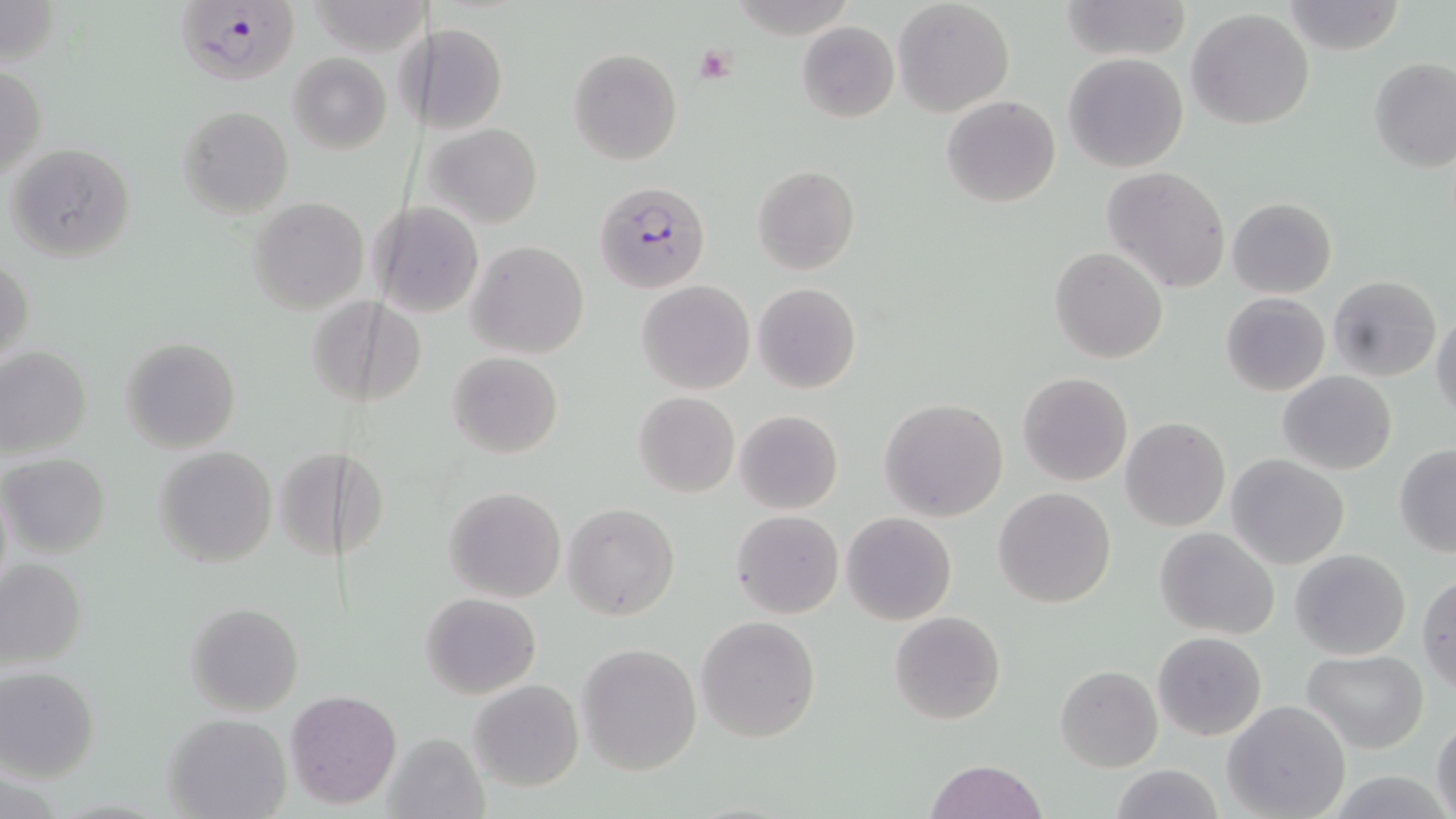 Approximate bounding boxes as named x1/y1/x2/y2 corners in pixels. Uninfected red blood cell locations: (x1=0, y1=0, x2=64, y2=68), (x1=893, y1=0, x2=1015, y2=116), (x1=1058, y1=0, x2=1191, y2=62), (x1=1281, y1=1, x2=1405, y2=54), (x1=1186, y1=8, x2=1316, y2=130), (x1=797, y1=20, x2=899, y2=123), (x1=394, y1=21, x2=427, y2=130), (x1=425, y1=23, x2=508, y2=134), (x1=568, y1=46, x2=683, y2=165), (x1=286, y1=53, x2=393, y2=154), (x1=1062, y1=53, x2=1189, y2=172), (x1=1367, y1=58, x2=1455, y2=172), (x1=1, y1=64, x2=45, y2=180), (x1=941, y1=95, x2=1060, y2=208), (x1=177, y1=104, x2=295, y2=219), (x1=423, y1=121, x2=546, y2=227), (x1=6, y1=142, x2=136, y2=262), (x1=752, y1=164, x2=860, y2=275), (x1=1103, y1=165, x2=1232, y2=293), (x1=248, y1=197, x2=369, y2=315), (x1=1227, y1=198, x2=1337, y2=297), (x1=370, y1=202, x2=485, y2=317), (x1=467, y1=241, x2=589, y2=358), (x1=1050, y1=246, x2=1167, y2=364), (x1=0, y1=256, x2=34, y2=368), (x1=1327, y1=275, x2=1441, y2=383), (x1=638, y1=281, x2=755, y2=395), (x1=753, y1=283, x2=861, y2=395), (x1=1221, y1=291, x2=1330, y2=397), (x1=309, y1=295, x2=425, y2=409), (x1=1431, y1=310, x2=1456, y2=421), (x1=119, y1=337, x2=242, y2=453), (x1=0, y1=346, x2=92, y2=460), (x1=447, y1=352, x2=563, y2=458), (x1=1277, y1=369, x2=1397, y2=475), (x1=1017, y1=372, x2=1133, y2=486), (x1=633, y1=391, x2=740, y2=498), (x1=879, y1=398, x2=1007, y2=522), (x1=734, y1=409, x2=842, y2=514), (x1=1121, y1=417, x2=1230, y2=531), (x1=1394, y1=444, x2=1456, y2=558), (x1=153, y1=446, x2=278, y2=569), (x1=277, y1=447, x2=341, y2=564), (x1=339, y1=448, x2=387, y2=564), (x1=1, y1=453, x2=110, y2=558), (x1=1227, y1=455, x2=1349, y2=569), (x1=442, y1=486, x2=566, y2=603), (x1=994, y1=487, x2=1115, y2=609), (x1=564, y1=502, x2=680, y2=621), (x1=732, y1=510, x2=844, y2=618), (x1=841, y1=512, x2=957, y2=625), (x1=1155, y1=527, x2=1278, y2=640), (x1=1290, y1=549, x2=1411, y2=661), (x1=0, y1=557, x2=87, y2=669), (x1=1418, y1=574, x2=1456, y2=692), (x1=421, y1=592, x2=541, y2=699), (x1=185, y1=601, x2=304, y2=715), (x1=888, y1=611, x2=1006, y2=725), (x1=696, y1=615, x2=821, y2=742), (x1=1153, y1=632, x2=1267, y2=741), (x1=577, y1=642, x2=703, y2=775), (x1=1301, y1=650, x2=1429, y2=754), (x1=1056, y1=665, x2=1162, y2=771), (x1=0, y1=667, x2=101, y2=781), (x1=467, y1=679, x2=585, y2=791), (x1=285, y1=689, x2=401, y2=809), (x1=1223, y1=700, x2=1353, y2=819), (x1=163, y1=711, x2=291, y2=818), (x1=1432, y1=717, x2=1456, y2=819), (x1=380, y1=731, x2=488, y2=819), (x1=924, y1=759, x2=1049, y2=818), (x1=1110, y1=765, x2=1223, y2=819), (x1=1323, y1=771, x2=1455, y2=819). Plasmodium falciparum-infected red blood cell locations: (x1=173, y1=1, x2=298, y2=89), (x1=596, y1=181, x2=710, y2=293). Platelet locations: (x1=692, y1=44, x2=739, y2=85). Slide-level diagnosis: Plasmodium falciparum. Image is 1456×819 pixels. Light microscopy. Captured at 1000x magnification. Thin blood film. May-Grünwald-Giemsa stain. One field of a larger specimen.